Give the extent of all Babesia divergens-infected red blood cells.
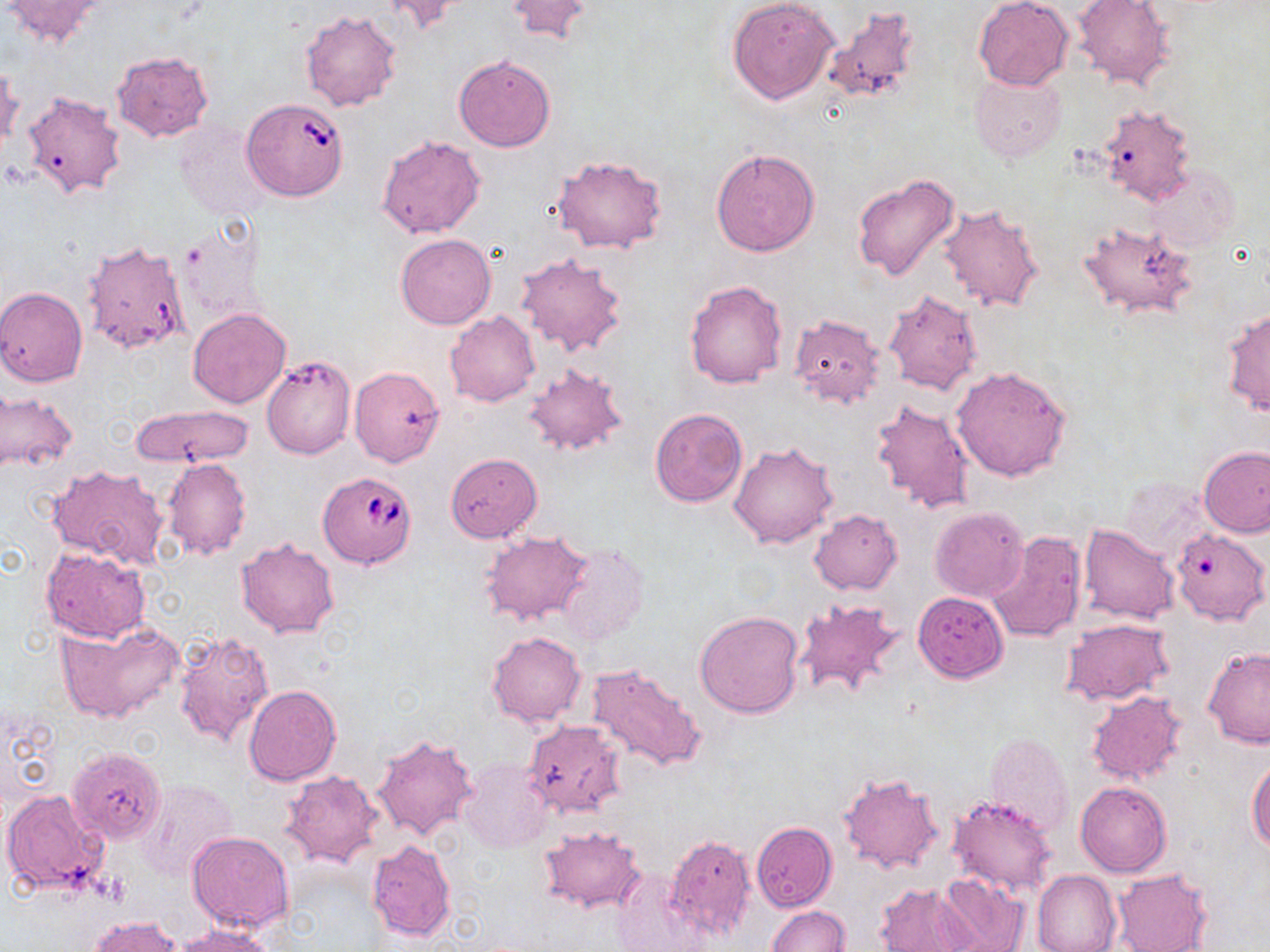

Approximate bounding boxes as named x1/y1/x2/y2 corners in pixels.
Babesia divergens-infected red blood cells: (x1=241, y1=97, x2=350, y2=202), (x1=318, y1=469, x2=419, y2=570).

Summary:
  - Uninfected red blood cell locations: (x1=377, y1=0, x2=471, y2=35), (x1=505, y1=0, x2=593, y2=45), (x1=727, y1=0, x2=841, y2=104), (x1=973, y1=0, x2=1073, y2=90), (x1=3, y1=1, x2=108, y2=47), (x1=1072, y1=1, x2=1176, y2=89), (x1=822, y1=7, x2=921, y2=105), (x1=299, y1=9, x2=403, y2=111), (x1=112, y1=51, x2=213, y2=141), (x1=453, y1=55, x2=556, y2=152), (x1=0, y1=62, x2=21, y2=153), (x1=970, y1=72, x2=1065, y2=162), (x1=22, y1=91, x2=126, y2=200), (x1=1096, y1=103, x2=1197, y2=206), (x1=173, y1=120, x2=272, y2=221), (x1=377, y1=135, x2=486, y2=238), (x1=710, y1=147, x2=820, y2=257), (x1=552, y1=154, x2=668, y2=253), (x1=1144, y1=163, x2=1240, y2=252), (x1=853, y1=173, x2=962, y2=282), (x1=938, y1=203, x2=1047, y2=314), (x1=1079, y1=220, x2=1198, y2=321), (x1=396, y1=234, x2=496, y2=329), (x1=82, y1=240, x2=189, y2=354), (x1=515, y1=251, x2=627, y2=358), (x1=684, y1=279, x2=788, y2=390), (x1=0, y1=286, x2=88, y2=386), (x1=883, y1=288, x2=983, y2=395), (x1=1224, y1=307, x2=1270, y2=415), (x1=188, y1=308, x2=292, y2=408), (x1=445, y1=311, x2=540, y2=408), (x1=789, y1=314, x2=885, y2=408), (x1=261, y1=356, x2=355, y2=459), (x1=523, y1=362, x2=629, y2=458), (x1=951, y1=365, x2=1071, y2=481), (x1=349, y1=366, x2=445, y2=466), (x1=0, y1=389, x2=75, y2=476), (x1=870, y1=398, x2=975, y2=515), (x1=127, y1=404, x2=255, y2=467), (x1=650, y1=407, x2=747, y2=507), (x1=729, y1=442, x2=839, y2=549), (x1=1200, y1=445, x2=1270, y2=537), (x1=445, y1=452, x2=542, y2=542), (x1=162, y1=457, x2=251, y2=560), (x1=47, y1=464, x2=169, y2=569), (x1=1120, y1=475, x2=1213, y2=564), (x1=929, y1=507, x2=1029, y2=602), (x1=810, y1=508, x2=902, y2=595), (x1=1079, y1=524, x2=1180, y2=624), (x1=1171, y1=529, x2=1269, y2=624), (x1=480, y1=531, x2=590, y2=627), (x1=986, y1=531, x2=1087, y2=643), (x1=236, y1=537, x2=339, y2=638), (x1=552, y1=543, x2=648, y2=645), (x1=41, y1=548, x2=149, y2=643), (x1=913, y1=592, x2=1008, y2=682), (x1=794, y1=595, x2=904, y2=701), (x1=694, y1=610, x2=804, y2=718), (x1=1061, y1=618, x2=1175, y2=706), (x1=56, y1=620, x2=184, y2=723), (x1=174, y1=629, x2=275, y2=752), (x1=487, y1=632, x2=585, y2=726), (x1=1202, y1=647, x2=1270, y2=747), (x1=587, y1=664, x2=704, y2=774), (x1=245, y1=685, x2=341, y2=785), (x1=1086, y1=690, x2=1188, y2=786), (x1=522, y1=720, x2=627, y2=819), (x1=982, y1=731, x2=1073, y2=837), (x1=370, y1=732, x2=478, y2=841), (x1=68, y1=747, x2=166, y2=841), (x1=1247, y1=756, x2=1270, y2=852), (x1=458, y1=759, x2=553, y2=853), (x1=280, y1=771, x2=384, y2=868), (x1=838, y1=771, x2=944, y2=876), (x1=135, y1=778, x2=239, y2=884), (x1=1075, y1=781, x2=1172, y2=877), (x1=2, y1=789, x2=111, y2=895), (x1=948, y1=795, x2=1060, y2=896), (x1=751, y1=822, x2=838, y2=913), (x1=537, y1=825, x2=646, y2=913), (x1=187, y1=831, x2=295, y2=932), (x1=665, y1=833, x2=756, y2=942), (x1=366, y1=841, x2=456, y2=941), (x1=611, y1=867, x2=706, y2=950), (x1=1032, y1=869, x2=1121, y2=952), (x1=934, y1=870, x2=1029, y2=952), (x1=1112, y1=871, x2=1211, y2=952), (x1=875, y1=883, x2=979, y2=951), (x1=766, y1=905, x2=850, y2=952), (x1=89, y1=916, x2=183, y2=952), (x1=171, y1=923, x2=282, y2=951)
  - Slide-level diagnosis: Babesia divergens
  - Stain: May-Grünwald-Giemsa
  - Magnification: 1000x
  - Modality: optical microscopy
  - Image size: 1270×952 pixels
  - Field of view: single
  - Preparation: thin blood film